Assess this cell for malaria.
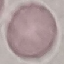
It is uninfected.

Photographed with a smartphone camera at the microscope eyepiece. Cell patch, automatically extracted from a larger field of view and resized to 64 × 64 pixels. Thin blood smear. Giemsa stain.